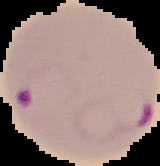
image type = segmented cell region with the area outside set to black
preparation = thin blood film
malaria status = parasitized
image size = 160×166 pixels